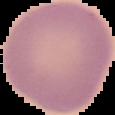

Summary:
  - Malaria status: uninfected
  - Image size: 115×115 pixels
  - Image type: segmented cell region with the area outside set to black
  - Preparation: thin blood smear